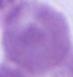
Summary:
  - Modality: micrograph
  - Magnification: 1000x
  - Identification: erythrocyte